Give the extent of all uninfected red blood cells.
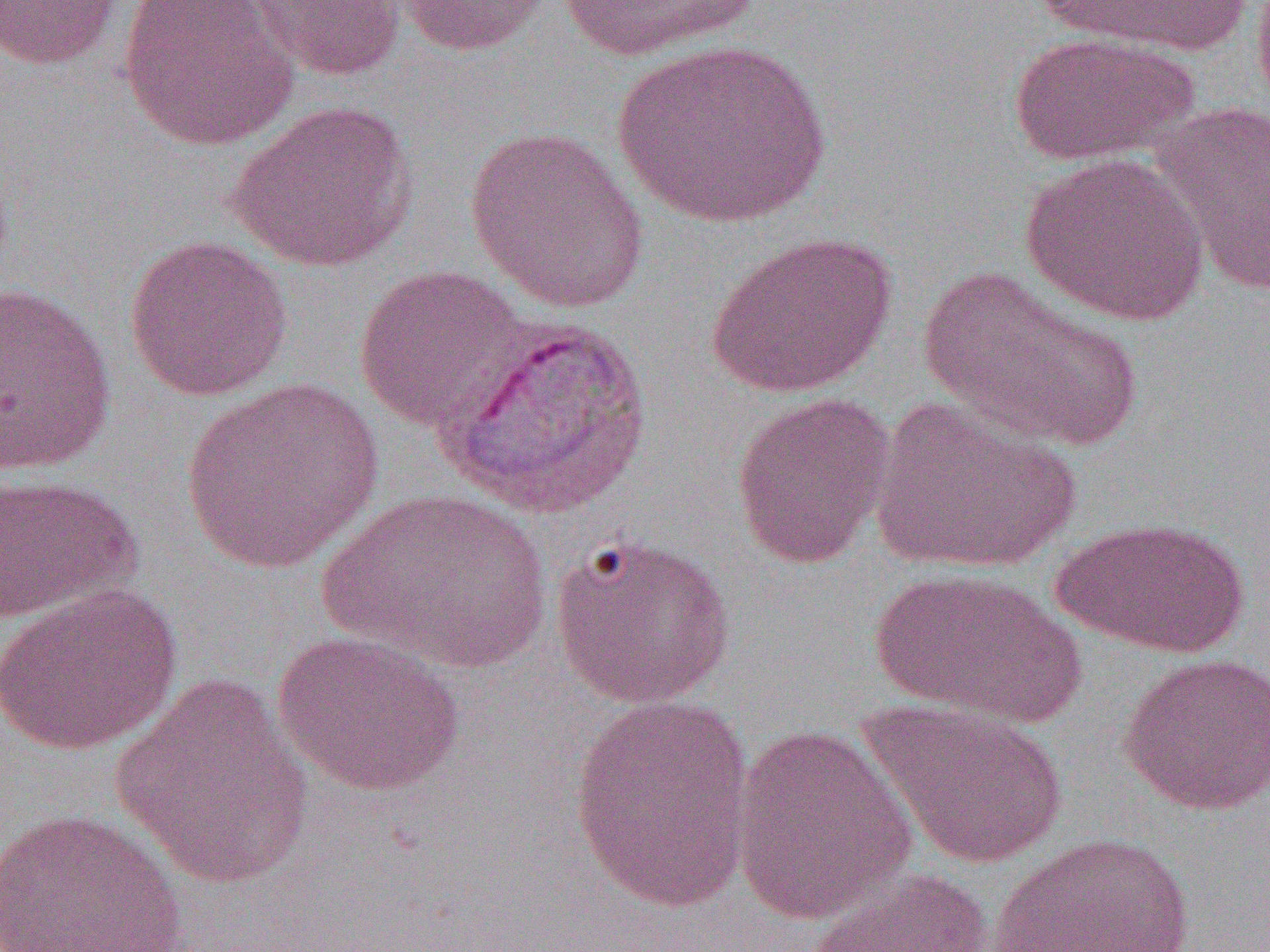

Approximate bounding boxes as named x1/y1/x2/y2 corners in pixels.
Uninfected red blood cells: (x1=0, y1=0, x2=126, y2=70), (x1=120, y1=0, x2=298, y2=151), (x1=241, y1=0, x2=407, y2=82), (x1=393, y1=0, x2=556, y2=56), (x1=1034, y1=0, x2=1254, y2=60), (x1=555, y1=1, x2=760, y2=63), (x1=1009, y1=32, x2=1200, y2=167), (x1=612, y1=39, x2=831, y2=229), (x1=1152, y1=99, x2=1270, y2=298), (x1=227, y1=100, x2=417, y2=271), (x1=463, y1=125, x2=650, y2=313), (x1=1019, y1=152, x2=1211, y2=325), (x1=706, y1=230, x2=896, y2=397), (x1=123, y1=234, x2=294, y2=402), (x1=353, y1=264, x2=530, y2=432), (x1=918, y1=264, x2=1142, y2=452), (x1=1, y1=281, x2=118, y2=475), (x1=180, y1=377, x2=383, y2=576), (x1=730, y1=391, x2=896, y2=570), (x1=868, y1=398, x2=1081, y2=575), (x1=0, y1=473, x2=142, y2=623), (x1=321, y1=489, x2=552, y2=673), (x1=1052, y1=516, x2=1251, y2=657), (x1=549, y1=532, x2=738, y2=710), (x1=868, y1=566, x2=1085, y2=726), (x1=0, y1=582, x2=182, y2=756), (x1=273, y1=628, x2=465, y2=797), (x1=1119, y1=652, x2=1270, y2=815), (x1=109, y1=674, x2=317, y2=889), (x1=568, y1=697, x2=757, y2=912), (x1=857, y1=697, x2=1068, y2=870), (x1=729, y1=722, x2=918, y2=925), (x1=0, y1=808, x2=190, y2=952), (x1=988, y1=832, x2=1198, y2=952), (x1=807, y1=868, x2=994, y2=952).

Summary:
  - Slide-level diagnosis: Plasmodium vivax
  - Image size: 1270×952 pixels
  - Field of view: one of a larger specimen
  - Preparation: thin blood smear
  - Magnification: 1000x
  - Modality: optical microscopy